State which parasite is depicted.
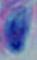

Toxoplasma gondii.

Summary:
  - Magnification: 1000x
  - Modality: micrograph